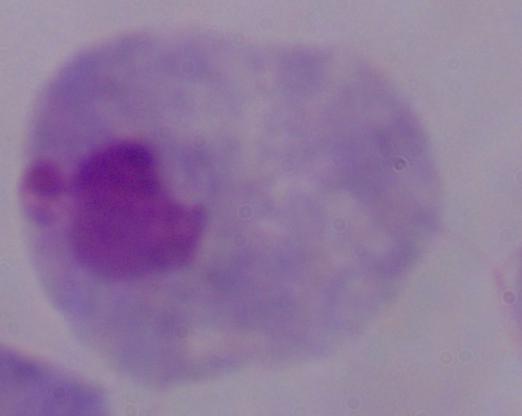

Summary:
  - Magnification: 1000x
  - Identification: trichomonad
  - Modality: photomicrograph